Describe the morphology of the red blood cells.
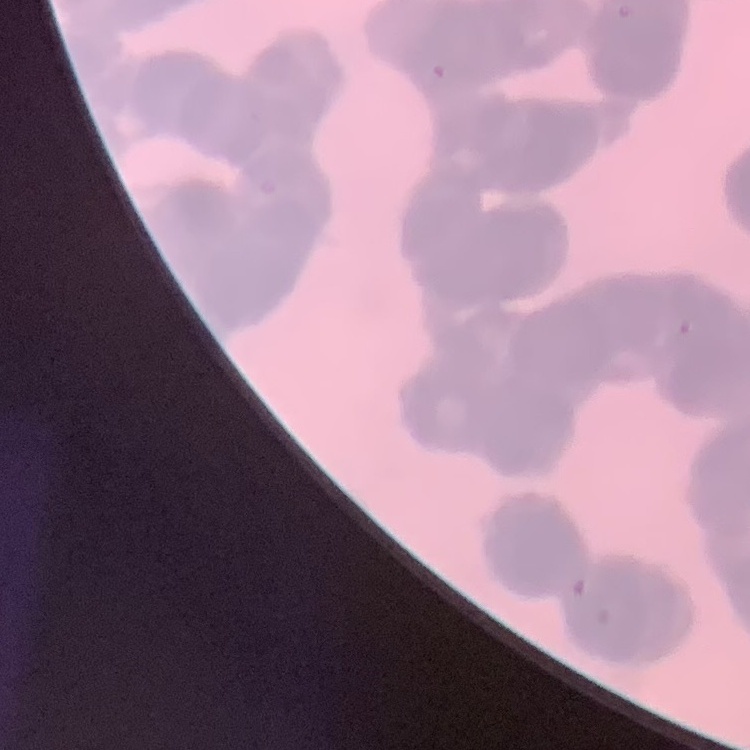

Rouleaux formation.

image type = one tile cut from a larger photomicrograph
preparation = thin blood film
stain = Field's or Giemsa